Name the parasite shown.
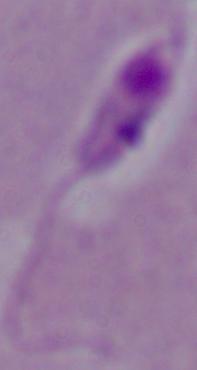
Leishmania.

Captured at 1000x magnification. Photomicrograph.